Classify this cell by malaria status.
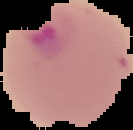

Parasitized.

Cell region segmented out of the field of view; the surrounding area is masked to black. From a thin blood smear. Image is 133×130 pixels.